State which cell type is depicted.
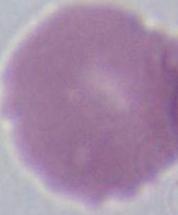

An erythrocyte.

Summary:
  - Magnification: 1000x
  - Modality: micrograph